Name the parasite shown.
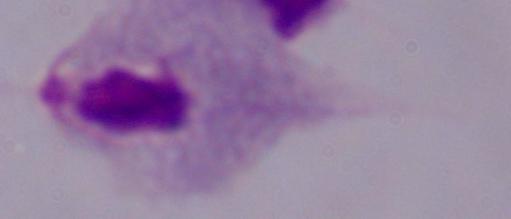
A trichomonad.

{
  "magnification": "1000x",
  "modality": "micrograph"
}